Give the preparation type.
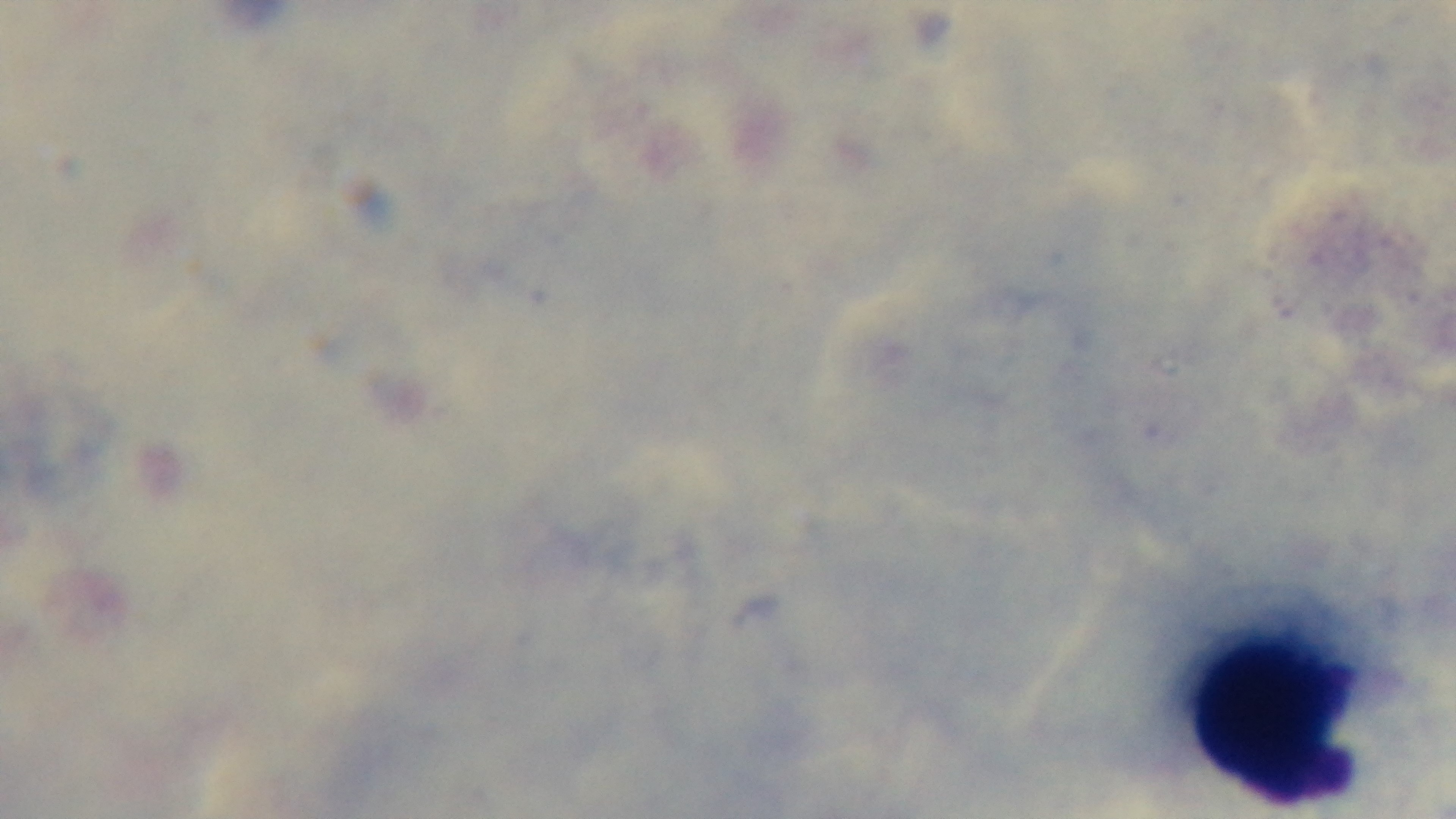
It is a thick blood film.

Light microscopy. Malaria status: negative. Giemsa stain. 100x oil-immersion objective. Mounted 4K digital camera. One field from the slide.